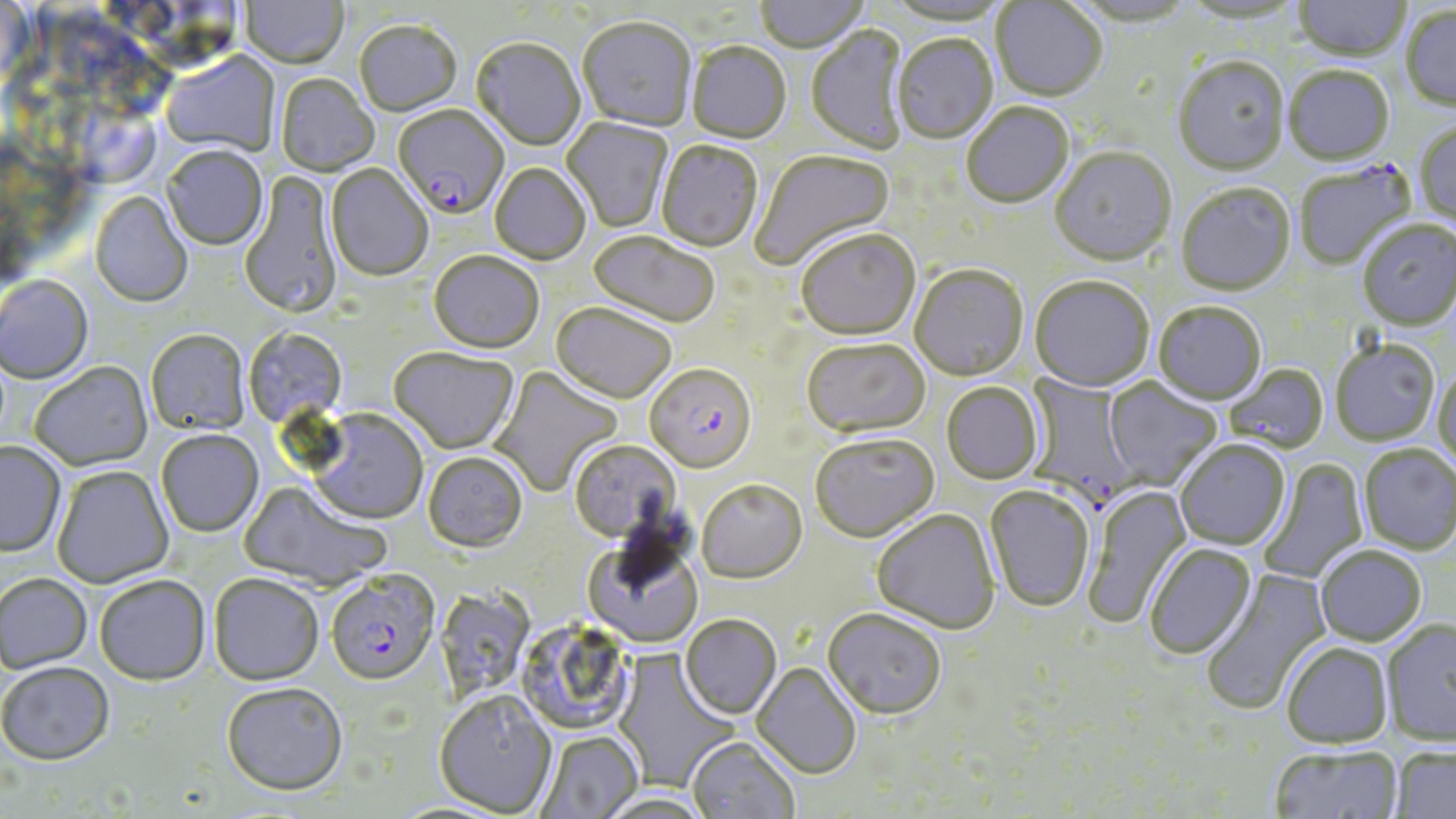

Summary:
  - Coordinate format: approximate bounding boxes as named x1/y1/x2/y2 corners in pixels
  - Plasmodium falciparum-infected red blood cell locations: (x1=393, y1=106, x2=509, y2=221), (x1=644, y1=366, x2=756, y2=476), (x1=1022, y1=374, x2=1138, y2=515), (x1=326, y1=573, x2=439, y2=689)
  - Uninfected red blood cell locations: (x1=241, y1=0, x2=348, y2=71), (x1=754, y1=0, x2=868, y2=55), (x1=885, y1=0, x2=1007, y2=28), (x1=1068, y1=0, x2=1196, y2=29), (x1=1180, y1=0, x2=1306, y2=26), (x1=991, y1=1, x2=1108, y2=104), (x1=1292, y1=1, x2=1410, y2=62), (x1=1401, y1=7, x2=1456, y2=114), (x1=578, y1=19, x2=696, y2=134), (x1=354, y1=22, x2=462, y2=118), (x1=806, y1=25, x2=911, y2=156), (x1=892, y1=36, x2=998, y2=146), (x1=471, y1=40, x2=586, y2=152), (x1=687, y1=44, x2=791, y2=145), (x1=161, y1=53, x2=280, y2=159), (x1=1172, y1=59, x2=1289, y2=178), (x1=1284, y1=68, x2=1395, y2=167), (x1=276, y1=75, x2=379, y2=178), (x1=961, y1=104, x2=1075, y2=211), (x1=562, y1=117, x2=672, y2=233), (x1=1415, y1=123, x2=1456, y2=229), (x1=656, y1=142, x2=763, y2=254), (x1=162, y1=148, x2=268, y2=251), (x1=1050, y1=149, x2=1176, y2=269), (x1=751, y1=151, x2=896, y2=271), (x1=1295, y1=162, x2=1416, y2=270), (x1=326, y1=165, x2=433, y2=283), (x1=490, y1=165, x2=590, y2=266), (x1=240, y1=171, x2=343, y2=322), (x1=1176, y1=186, x2=1296, y2=298), (x1=90, y1=192, x2=192, y2=309), (x1=1358, y1=222, x2=1456, y2=332), (x1=797, y1=231, x2=921, y2=343), (x1=588, y1=232, x2=719, y2=330), (x1=428, y1=254, x2=544, y2=355), (x1=909, y1=266, x2=1028, y2=383), (x1=0, y1=277, x2=94, y2=385), (x1=1030, y1=278, x2=1154, y2=394), (x1=1153, y1=303, x2=1266, y2=407), (x1=550, y1=305, x2=676, y2=406), (x1=244, y1=329, x2=347, y2=429), (x1=146, y1=331, x2=250, y2=437), (x1=803, y1=340, x2=931, y2=441), (x1=1332, y1=342, x2=1440, y2=447), (x1=389, y1=348, x2=519, y2=455), (x1=29, y1=363, x2=153, y2=472), (x1=488, y1=365, x2=623, y2=498), (x1=1224, y1=365, x2=1330, y2=456), (x1=1433, y1=367, x2=1456, y2=473), (x1=1102, y1=377, x2=1222, y2=492), (x1=942, y1=384, x2=1044, y2=485), (x1=306, y1=410, x2=428, y2=526), (x1=156, y1=431, x2=264, y2=538), (x1=809, y1=435, x2=940, y2=546), (x1=568, y1=441, x2=681, y2=547), (x1=1175, y1=441, x2=1290, y2=552), (x1=0, y1=443, x2=66, y2=558), (x1=1358, y1=445, x2=1456, y2=556), (x1=423, y1=452, x2=527, y2=553), (x1=1258, y1=459, x2=1368, y2=584), (x1=52, y1=467, x2=174, y2=589), (x1=239, y1=481, x2=390, y2=593), (x1=697, y1=482, x2=807, y2=585), (x1=1085, y1=485, x2=1193, y2=628), (x1=984, y1=487, x2=1094, y2=614), (x1=872, y1=511, x2=1000, y2=637), (x1=583, y1=539, x2=703, y2=650), (x1=1144, y1=544, x2=1257, y2=660), (x1=1316, y1=547, x2=1426, y2=647), (x1=1200, y1=568, x2=1332, y2=715), (x1=0, y1=575, x2=93, y2=675), (x1=209, y1=575, x2=324, y2=688), (x1=95, y1=578, x2=210, y2=688), (x1=442, y1=584, x2=540, y2=703), (x1=822, y1=610, x2=947, y2=722), (x1=680, y1=616, x2=782, y2=720), (x1=520, y1=620, x2=634, y2=731), (x1=1381, y1=621, x2=1456, y2=748), (x1=1281, y1=642, x2=1393, y2=748), (x1=612, y1=649, x2=740, y2=794), (x1=752, y1=663, x2=861, y2=780), (x1=0, y1=665, x2=115, y2=768), (x1=221, y1=684, x2=348, y2=799), (x1=434, y1=693, x2=557, y2=817), (x1=535, y1=731, x2=643, y2=819), (x1=687, y1=738, x2=800, y2=819), (x1=1268, y1=745, x2=1404, y2=819), (x1=1391, y1=746, x2=1456, y2=818), (x1=594, y1=792, x2=714, y2=819)
  - Slide-level diagnosis: Plasmodium falciparum
  - Image size: 1456×819 pixels
  - Stain: May-Grünwald-Giemsa
  - Field of view: single
  - Preparation: thin blood film
  - Modality: optical microscopy
  - Magnification: 1000x